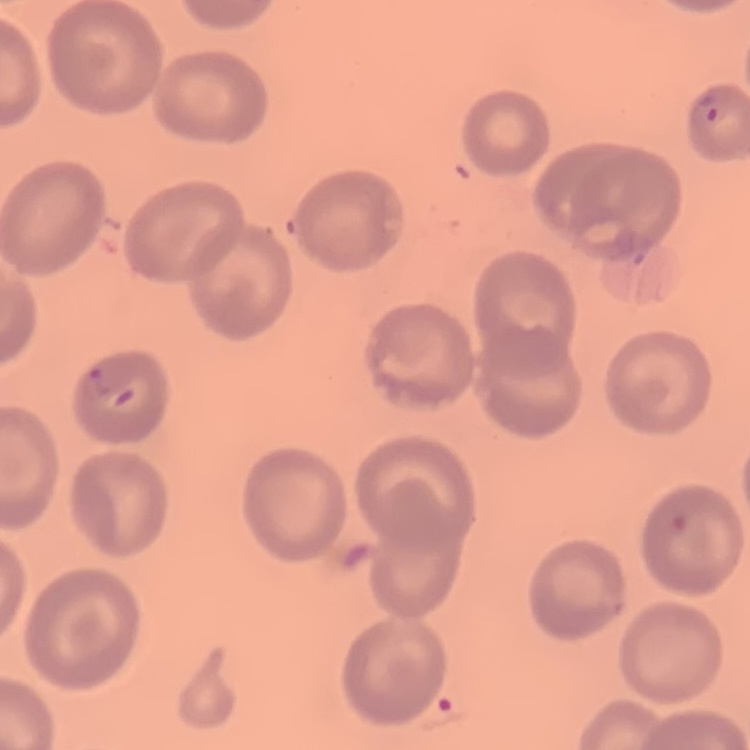

{
  "red_blood_cell_morphology": "no rouleaux formation",
  "image_type": "square crop of a larger photomicrograph",
  "preparation": "thin peripheral smear",
  "stain": "Field's or Giemsa"
}